Find each parasitized RBC.
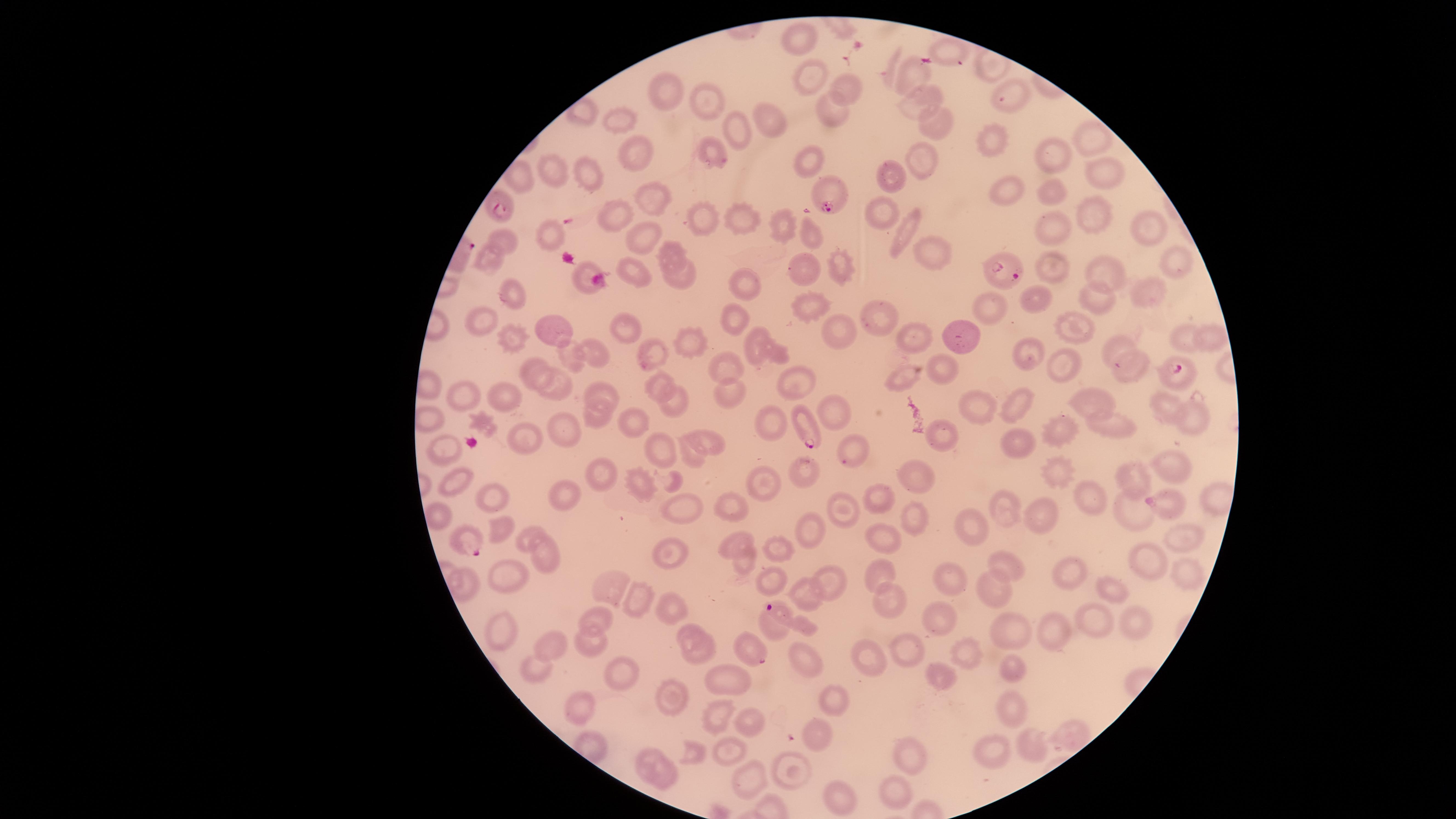
Approximate marker points as {x, y} in pixels.
Parasitized RBCs: {829, 189}, {503, 205}, {1005, 275}, {1174, 368}, {805, 425}, {1161, 504}, {464, 539}, {769, 608}, {753, 653}.

Approximate marker points as {x, y} in pixels. Uninfected RBCs: {803, 40}, {952, 48}, {811, 72}, {914, 79}, {840, 87}, {676, 88}, {707, 95}, {916, 102}, {833, 112}, {616, 114}, {771, 119}, {731, 123}, {930, 124}, {1091, 138}, {986, 140}, {713, 152}, {633, 155}, {1052, 161}, {812, 162}, {923, 165}, {1106, 172}, {520, 173}, {555, 174}, {590, 174}, {897, 175}, {1049, 191}, {1000, 193}, {659, 196}, {618, 207}, {881, 211}, {739, 218}, {1094, 219}, {779, 226}, {1138, 227}, {806, 230}, {1049, 230}, {905, 235}, {554, 237}, {502, 241}, {642, 241}, {934, 248}, {672, 253}, {493, 260}, {1170, 261}, {837, 264}, {1057, 265}, {807, 272}, {1107, 272}, {638, 273}, {679, 277}, {739, 286}, {1153, 290}, {513, 295}, {1092, 302}, {815, 304}, {1031, 308}, {988, 313}, {881, 314}, {485, 321}, {731, 323}, {1077, 327}, {549, 328}, {627, 329}, {837, 332}, {1187, 337}, {1206, 337}, {920, 338}, {513, 339}, {961, 340}, {688, 343}, {751, 347}, {1114, 348}, {771, 349}, {597, 350}, {656, 354}, {1032, 355}, {577, 360}, {1060, 365}, {1139, 365}, {534, 369}, {943, 371}, {724, 372}, {908, 373}, {798, 378}, {666, 383}, {561, 387}, {602, 389}, {730, 392}, {473, 395}, {508, 398}, {1089, 403}, {679, 405}, {986, 406}, {1014, 406}, {1167, 408}, {831, 411}, {593, 415}, {427, 419}, {1194, 420}, {634, 421}, {766, 423}, {1115, 425}, {564, 428}, {1064, 431}, {944, 435}, {525, 437}, {1019, 441}, {714, 443}, {664, 449}, {854, 449}, {692, 452}, {446, 453}, {1169, 464}, {801, 466}, {1057, 471}, {923, 473}, {593, 476}, {767, 481}, {1140, 481}, {455, 486}, {637, 487}, {880, 497}, {1094, 497}, {500, 499}, {565, 499}, {733, 505}, {1136, 507}, {842, 508}, {1009, 509}, {676, 511}, {435, 515}, {1048, 515}, {915, 519}, {498, 526}, {814, 529}, {887, 532}, {969, 533}, {739, 539}, {1184, 540}, {524, 541}, {784, 547}, {544, 552}, {669, 554}, {1149, 559}, {746, 561}, {1009, 565}, {1069, 568}, {1179, 569}, {885, 573}, {829, 577}, {949, 581}, {510, 583}, {777, 585}, {609, 586}, {998, 588}, {810, 590}, {1110, 590}, {634, 597}, {890, 597}, {670, 605}, {602, 618}, {934, 619}, {1096, 621}, {1130, 625}, {692, 630}, {1048, 631}, {1002, 632}, {507, 633}, {594, 644}, {958, 648}, {552, 650}, {902, 651}, {699, 656}, {803, 656}, {865, 660}, {931, 670}, {532, 672}, {1015, 673}, {619, 677}, {731, 681}, {676, 699}, {832, 702}, {1015, 706}, {583, 710}, {712, 719}, {746, 728}, {1063, 735}, {819, 737}, {1032, 743}, {731, 749}, {697, 750}, {994, 753}, {910, 755}, {799, 767}, {655, 779}, {751, 783}, {894, 794}, {843, 795}. The visible region is circular. Species: Plasmodium falciparum. Thin smear of blood. Giemsa stain. One field of view of the specimen. Image is 1456×819 pixels. Smartphone photograph through the microscope eyepiece.